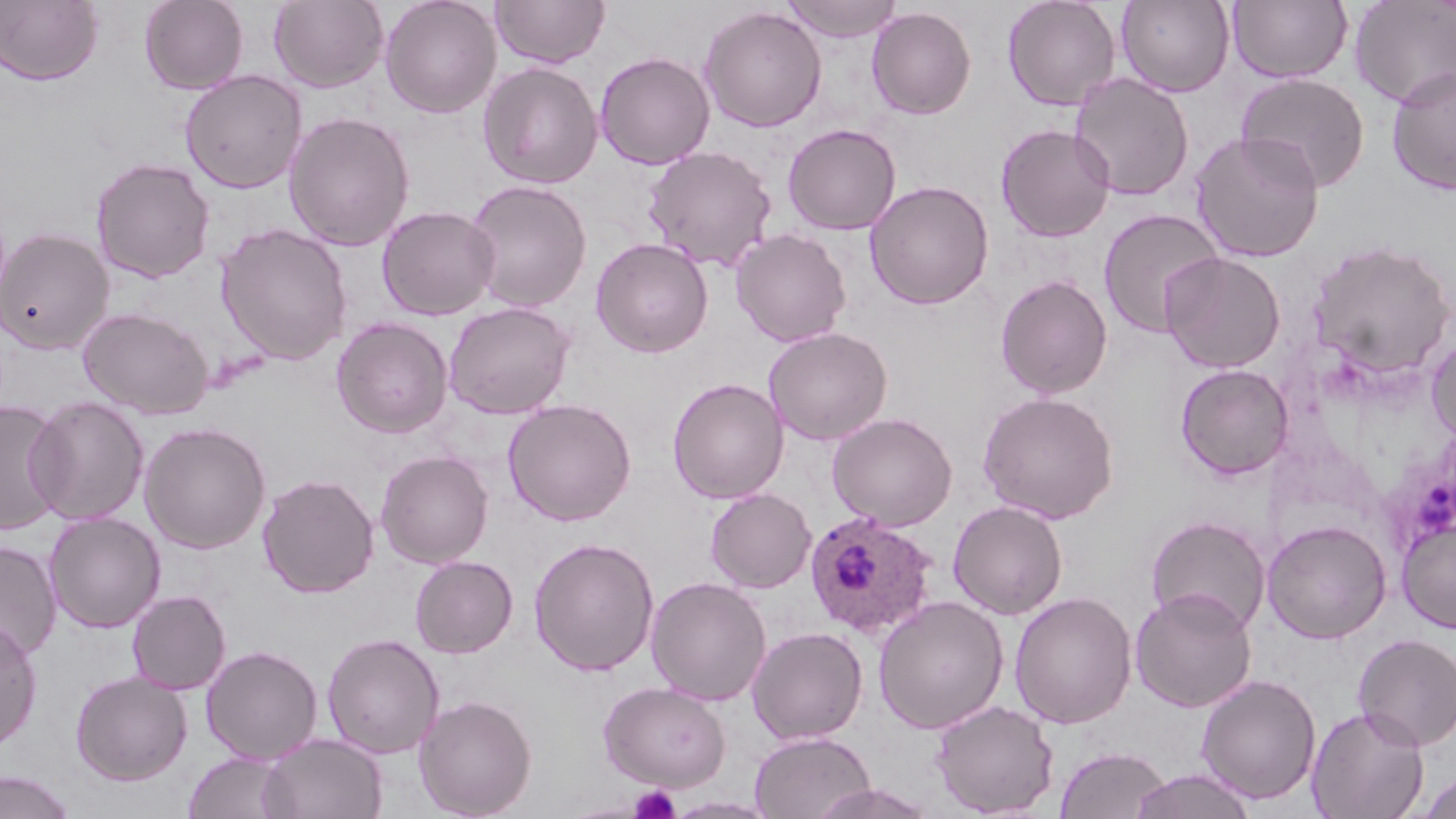
Approximate bounding boxes as (x1,y1)-(x2,y2) corner pairs in pixels. Plasmodium ovale-infected red blood cell locations: (803,510)-(938,639). Platelet locations: (629,785)-(681,819). Uninfected red blood cell locations: (139,0)-(249,94), (269,0)-(388,92), (380,0)-(502,118), (490,0)-(610,68), (782,0)-(903,43), (1002,0)-(1120,111), (1116,0)-(1235,97), (1227,0)-(1352,84), (1349,0)-(1456,109), (0,1)-(103,86), (699,6)-(827,132), (866,6)-(976,119), (595,52)-(715,170), (478,61)-(604,189), (1385,65)-(1456,195), (179,70)-(307,194), (1069,72)-(1194,201), (1236,72)-(1370,192), (283,111)-(415,251), (995,123)-(1116,242), (782,124)-(901,235), (1189,130)-(1325,263), (643,145)-(777,272), (91,157)-(216,284), (464,180)-(592,312), (865,180)-(994,310), (377,205)-(500,320), (1098,207)-(1226,339), (216,223)-(353,366), (0,226)-(114,354), (731,228)-(851,347), (591,237)-(713,358), (1308,238)-(1455,379), (1160,251)-(1286,373), (994,274)-(1113,399), (443,301)-(575,419), (78,307)-(213,419), (331,317)-(454,438), (763,327)-(892,445), (1426,334)-(1456,445), (1174,363)-(1293,480), (667,377)-(789,504), (978,390)-(1119,524), (26,395)-(150,526), (0,398)-(69,535), (502,398)-(637,526), (827,412)-(957,531), (138,422)-(271,553), (375,450)-(494,568), (258,473)-(379,598), (705,488)-(816,593), (948,499)-(1068,620), (44,512)-(165,633), (1145,514)-(1272,635), (1397,516)-(1456,633), (1262,519)-(1392,643), (529,537)-(659,676), (0,539)-(61,662), (410,555)-(519,658), (646,576)-(772,706), (1130,587)-(1257,712), (127,590)-(231,694), (1009,591)-(1137,729), (873,595)-(1009,733), (0,619)-(43,752), (747,626)-(869,745), (321,632)-(445,759), (1353,633)-(1456,750), (200,645)-(324,764), (69,671)-(193,786), (1196,673)-(1322,804), (599,681)-(730,791), (413,694)-(537,819), (930,699)-(1060,817), (1306,706)-(1430,819), (749,731)-(875,819), (259,733)-(388,819), (1054,745)-(1172,819), (182,751)-(295,819), (1130,768)-(1258,819), (0,770)-(77,819), (1415,771)-(1455,819). Slide-level diagnosis: Plasmodium ovale. Light microscopy. Image is 1456×819 pixels. Single field of view. May-Grünwald-Giemsa-stained preparation. Thin blood smear. 1000x magnification.